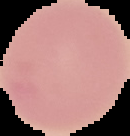 Image is 130×136 pixels. Segmented cell region on a black background. Result: no Plasmodium parasites seen. From a thin blood film.